Comment on the morphology of the erythrocytes.
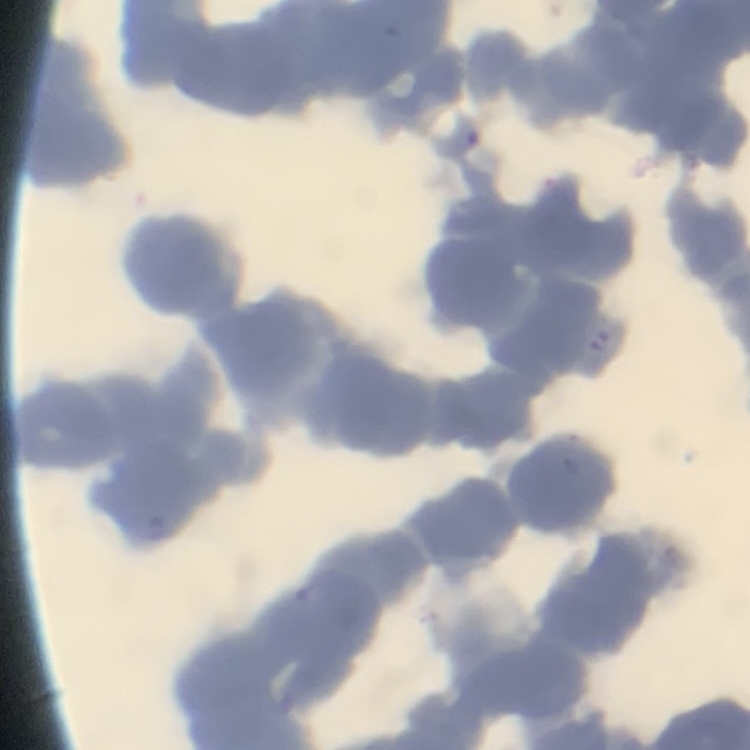
Rouleaux formation.

Thin blood film. Field's or Giemsa stain. One tile cut from a larger photomicrograph.